Report the malaria status of this cell.
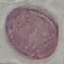

Uninfected.

Cell patch, automatically extracted from a larger field of view and resized to 64 × 64 pixels. Acquired by smartphone through the microscope eyepiece. Giemsa stain. Thin blood film.